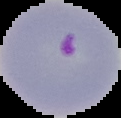
Image is 121×118 pixels. From a thin blood smear. The area outside the segmented cell region is set to black. Malaria status: parasitized.